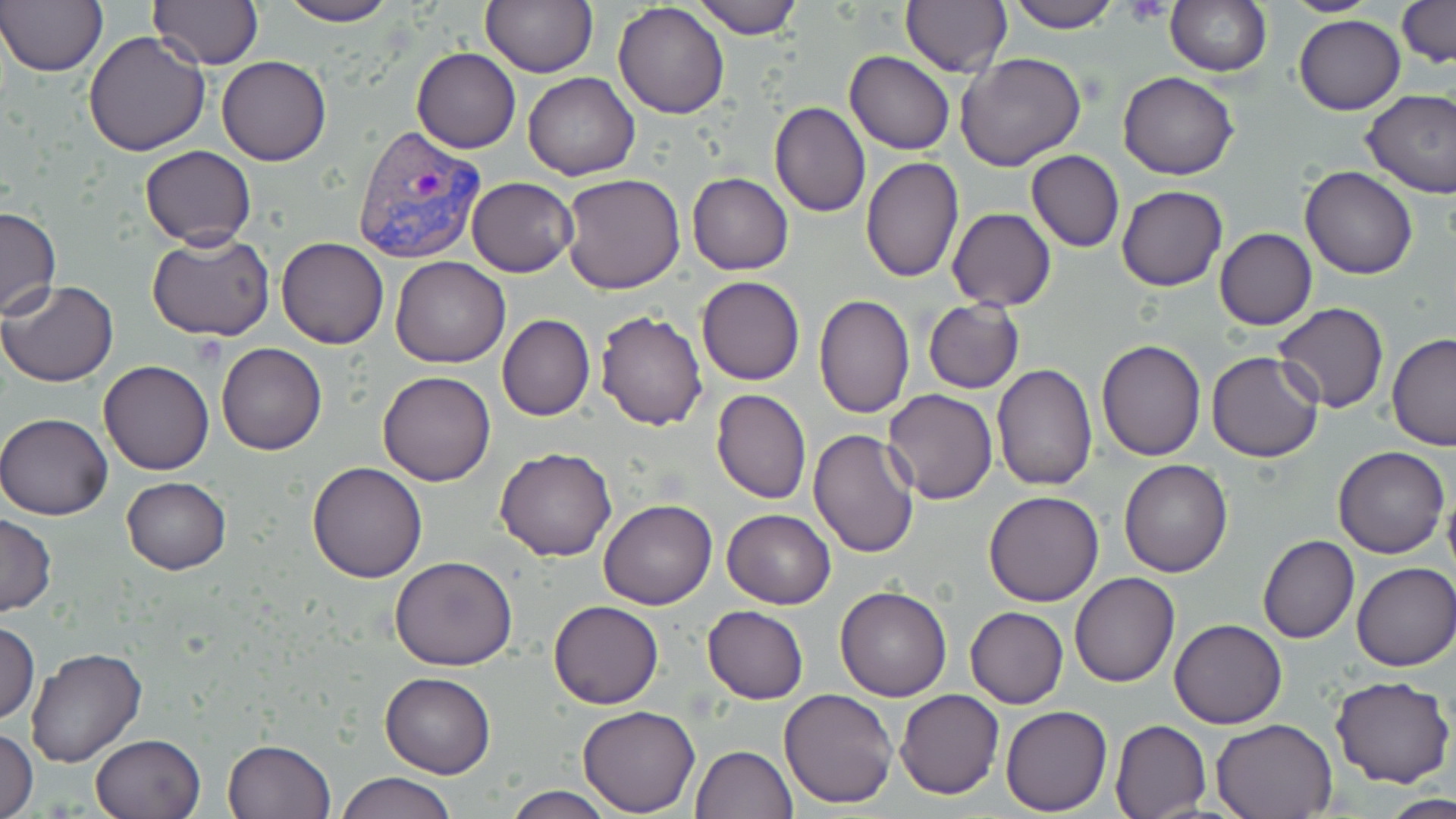

slide-level diagnosis = Plasmodium vivax
field of view = one of a larger specimen
stain = May-Grünwald-Giemsa
preparation = thin blood film
Plasmodium vivax-infected red blood cell locations = approximate bounding boxes as (x1,y1)-(x2,y2) corner pairs in pixels: (353,125)-(487,263)
modality = light microscopy
magnification = 1000x
uninfected red blood cell locations = approximate bounding boxes as (x1,y1)-(x2,y2) corner pairs in pixels: (0,0)-(109,76), (277,0)-(400,26), (480,0)-(597,77), (693,0)-(803,38), (901,0)-(1011,76), (1006,0)-(1121,33), (1276,0)-(1388,16), (1395,0)-(1455,70), (613,1)-(730,120), (1165,1)-(1272,77), (150,2)-(265,69), (1293,14)-(1405,114), (83,31)-(211,155), (411,46)-(522,154), (845,50)-(955,155), (956,53)-(1087,172), (216,55)-(331,165), (1119,70)-(1238,180), (523,72)-(640,180), (1361,88)-(1456,198), (769,102)-(871,218), (139,145)-(256,247), (1026,150)-(1125,252), (861,155)-(965,284), (1299,165)-(1418,280), (562,173)-(686,294), (687,173)-(794,274), (465,176)-(578,276), (1116,185)-(1227,292), (0,205)-(60,319), (947,208)-(1056,311), (1214,228)-(1318,330), (146,231)-(276,344), (276,238)-(388,349), (391,256)-(509,366), (696,276)-(805,386), (1,281)-(118,385), (814,295)-(914,419), (920,298)-(1026,395), (1273,302)-(1389,413), (595,310)-(708,431), (497,314)-(595,421), (1386,331)-(1456,451), (1096,338)-(1206,460), (216,342)-(328,455), (1206,351)-(1323,462), (98,359)-(214,474), (992,363)-(1098,491), (378,370)-(495,486), (711,388)-(811,504), (883,389)-(998,504), (0,412)-(112,521), (807,427)-(921,558), (1334,446)-(1449,559), (495,447)-(617,561), (1118,459)-(1233,578), (308,461)-(428,583), (121,476)-(231,574), (1442,487)-(1456,582), (982,491)-(1105,606), (598,499)-(717,610), (722,508)-(835,608), (0,513)-(58,616), (1258,534)-(1360,644), (390,555)-(518,672), (1351,562)-(1455,672), (1069,573)-(1180,688), (834,583)-(952,702), (548,600)-(664,710), (702,605)-(809,704), (965,607)-(1069,709), (1170,618)-(1287,729), (0,622)-(39,725), (24,646)-(147,768), (380,672)-(495,777), (1330,676)-(1454,788), (778,687)-(899,808), (895,688)-(1004,799), (1001,705)-(1111,815), (578,706)-(701,816), (1210,718)-(1338,819), (1110,720)-(1211,819), (0,728)-(38,819), (90,732)-(206,819), (222,738)-(335,818), (688,745)-(797,819), (336,772)-(458,819), (501,785)-(615,819), (1381,795)-(1456,818)
image size = 1456×819 pixels